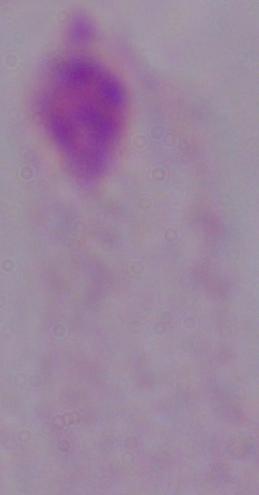
modality = photomicrograph
magnification = 1000x
identification = trichomonad